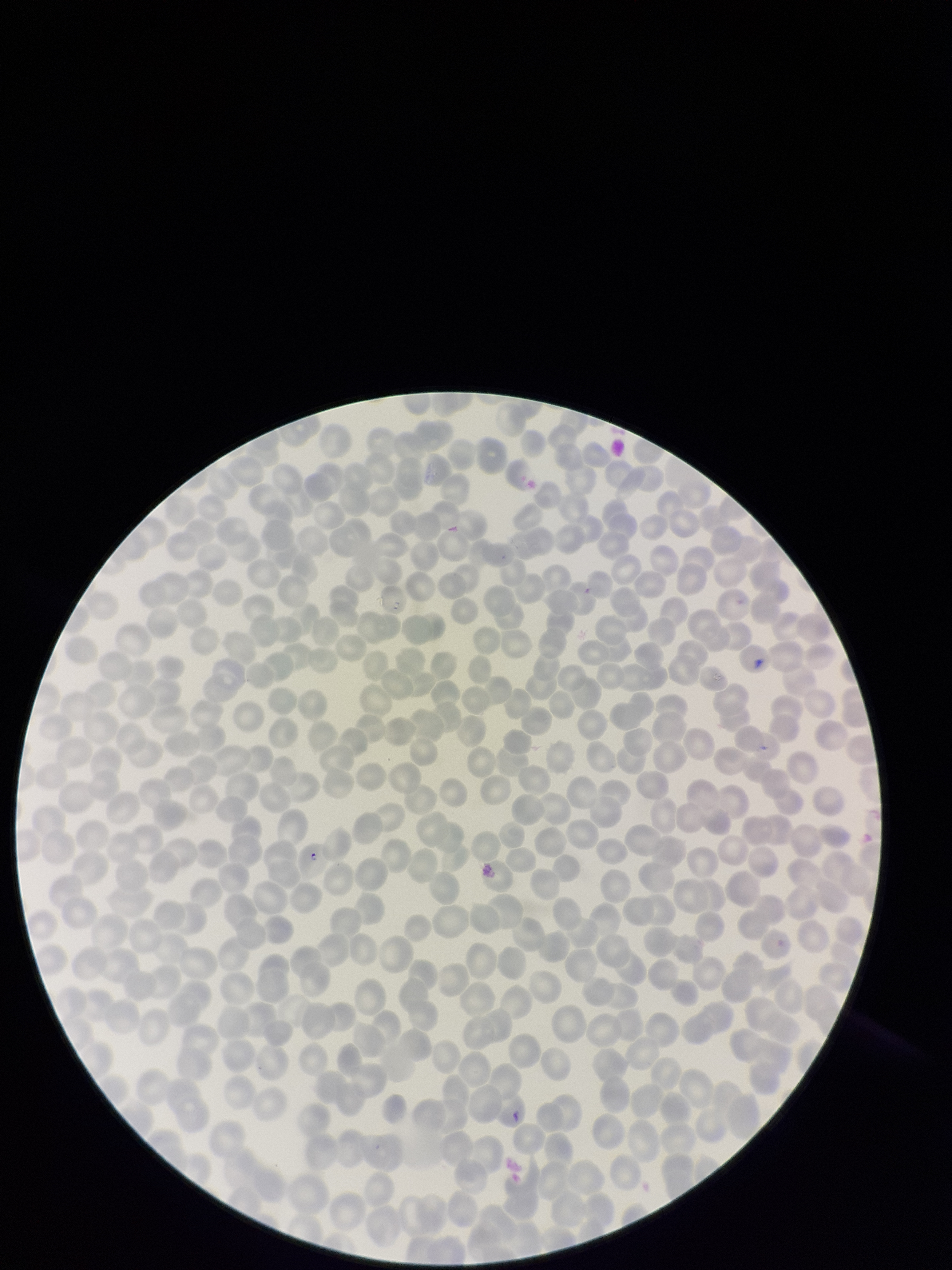
image size = 952×1270 pixels
red blood cell count = 395
preparation = thin
capture = smartphone photograph through the microscope eyepiece
stain = Giemsa
field of view = one from this slide
patient malaria status = positive
parasitized red blood cells = seen
species reported for this patient = Plasmodium falciparum
parasitized red blood cell count = 1